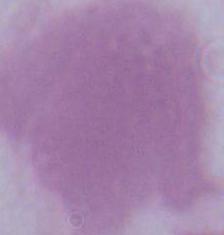
Summary:
  - Magnification: 1000x
  - Modality: micrograph
  - Identification: erythrocyte